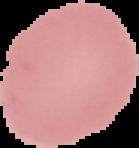
image_type: segmented cell region with the area outside set to black
preparation: thin blood smear
malaria_status: uninfected
image_size: 139×148 pixels